Outline each Plasmodium ovale-infected red blood cell.
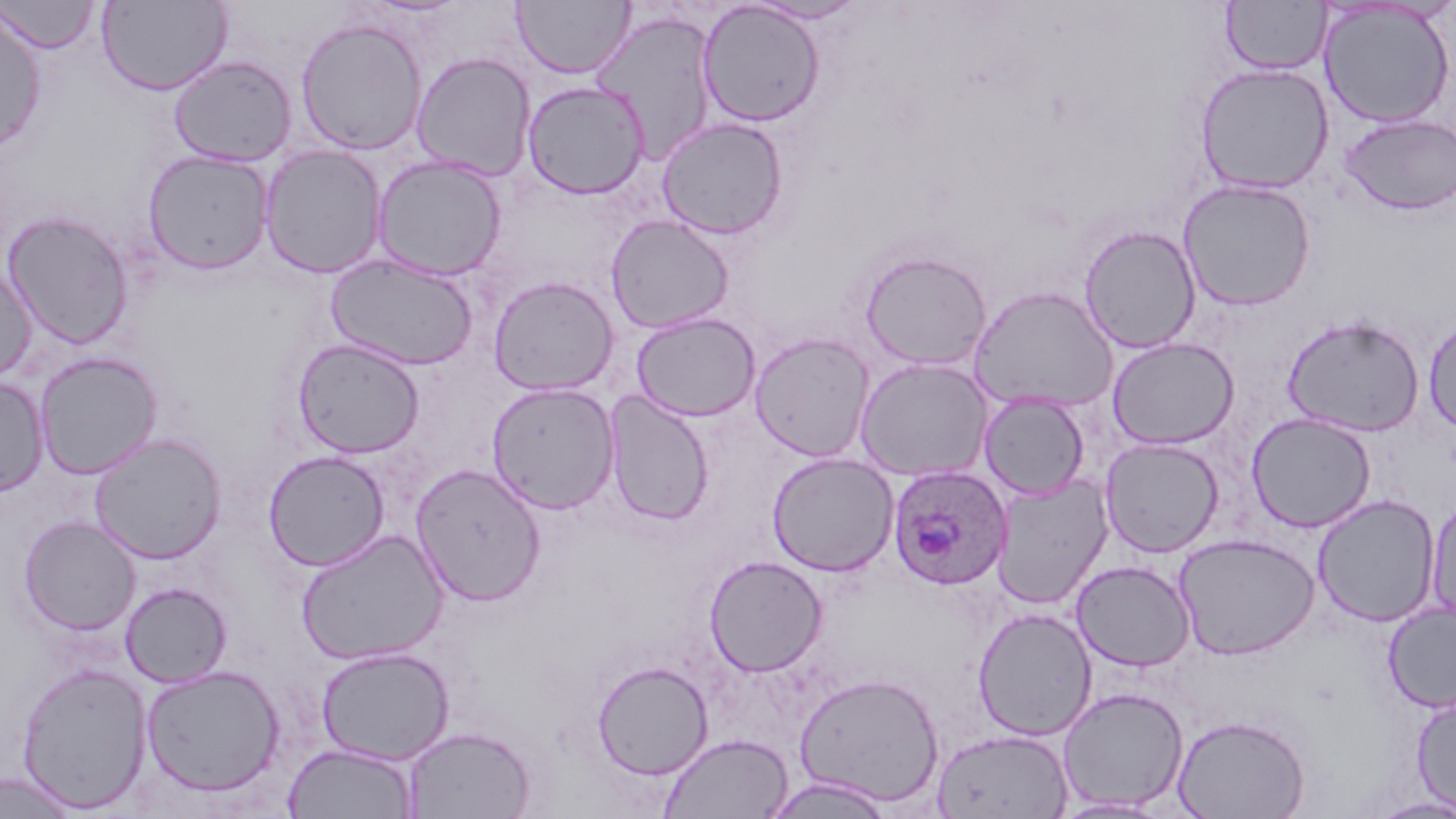

Approximate bounding boxes as (x1, y1, x2, y2) in pixels.
Plasmodium ovale-infected red blood cells: (887, 465, 1013, 590).

Summary:
  - Uninfected red blood cell locations: (1, 0, 101, 54), (513, 0, 635, 79), (743, 0, 870, 24), (96, 1, 233, 95), (1221, 1, 1331, 75), (697, 2, 826, 127), (1318, 2, 1455, 128), (0, 10, 46, 150), (591, 10, 718, 165), (294, 17, 428, 156), (410, 52, 535, 181), (169, 55, 296, 167), (1195, 62, 1335, 195), (522, 80, 650, 199), (1339, 113, 1456, 216), (656, 117, 789, 240), (259, 145, 387, 279), (142, 150, 275, 275), (372, 155, 507, 281), (1178, 178, 1316, 311), (2, 211, 135, 350), (606, 215, 735, 333), (1079, 224, 1202, 353), (859, 250, 992, 371), (325, 254, 479, 371), (0, 266, 37, 383), (488, 276, 619, 395), (968, 286, 1119, 413), (631, 312, 760, 421), (1282, 314, 1426, 437), (1422, 314, 1456, 436), (750, 331, 875, 462), (292, 337, 425, 458), (1107, 337, 1239, 450), (33, 351, 163, 479), (854, 358, 995, 482), (0, 376, 49, 497), (486, 381, 620, 514), (977, 391, 1090, 500), (603, 392, 715, 526), (1246, 412, 1377, 533), (89, 433, 226, 564), (1100, 438, 1224, 557), (263, 450, 390, 571), (766, 452, 899, 576), (411, 463, 546, 606), (991, 477, 1112, 609), (1312, 494, 1441, 627), (1427, 494, 1456, 630), (19, 516, 141, 636), (296, 529, 450, 666), (1174, 533, 1320, 659), (704, 555, 827, 676), (1071, 560, 1196, 671), (120, 582, 232, 688), (1382, 601, 1456, 714), (972, 607, 1098, 740), (316, 646, 455, 764), (591, 660, 713, 780), (16, 662, 152, 813), (140, 664, 286, 798), (794, 672, 945, 808), (1057, 686, 1189, 812), (1411, 694, 1456, 814), (1171, 714, 1311, 819), (403, 725, 537, 819), (932, 728, 1073, 819), (659, 733, 793, 819), (282, 742, 418, 818), (0, 771, 80, 818), (764, 775, 897, 818), (1368, 795, 1456, 818), (1051, 797, 1173, 818)
  - Slide-level diagnosis: Plasmodium ovale
  - Magnification: 1000x
  - Preparation: thin blood film
  - Image size: 1456×819 pixels
  - Modality: light microscopy
  - Field of view: one of a larger specimen
  - Stain: May-Grünwald-Giemsa